Report the malaria status of this cell.
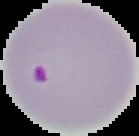

It is parasitized.

Summary:
  - Preparation: thin blood smear
  - Image type: segmented cell region on a black background
  - Image size: 139×136 pixels